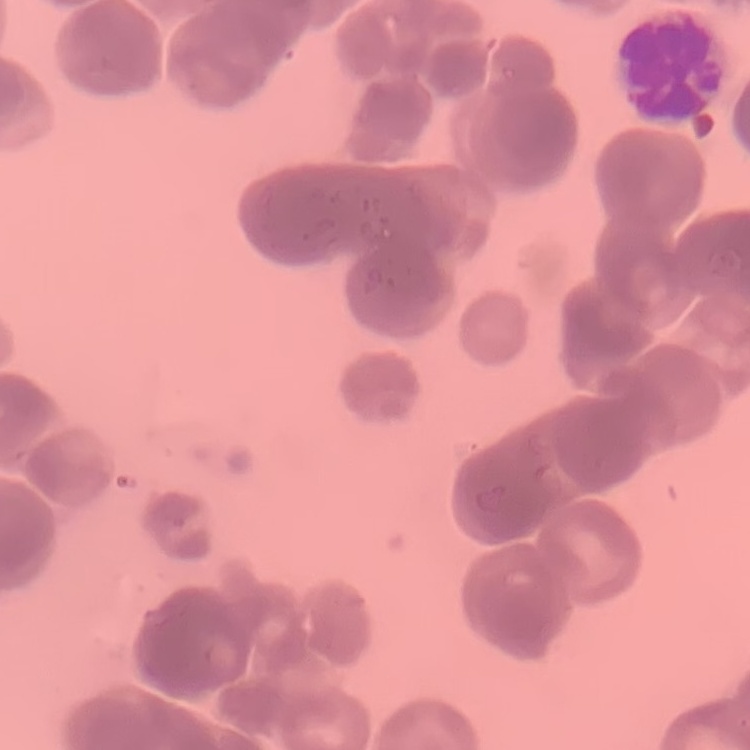

The erythrocytes show rouleaux formation. Square crop of a larger photomicrograph. Field's or Giemsa stain. Thin blood smear.